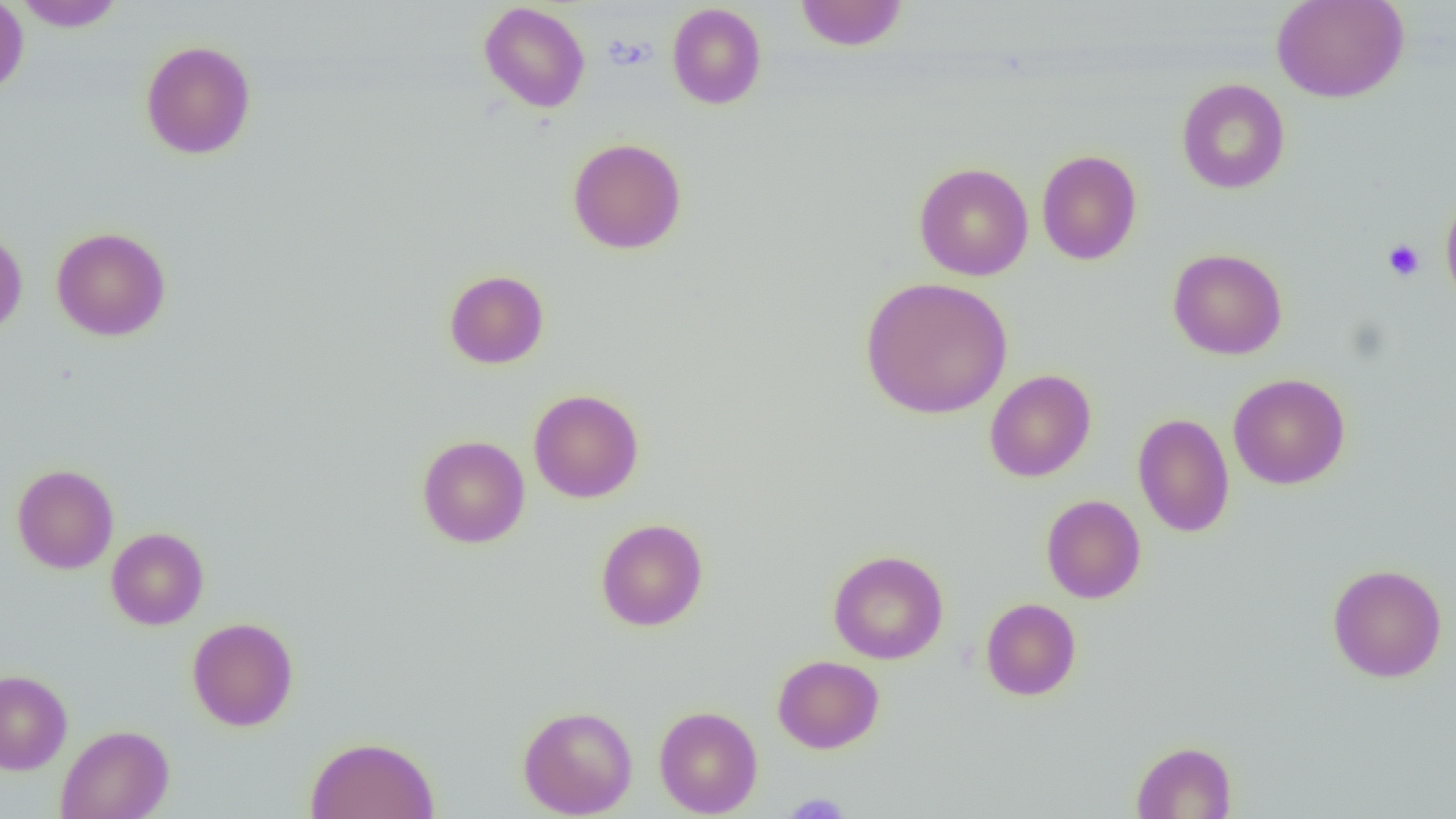
Summary:
  - Coordinate format: approximate bounding boxes as (x1,y1)-(x2,y2) corner pairs in pixels
  - Uninfected red blood cell locations: (0,0)-(29,96), (12,0)-(126,31), (795,0)-(907,51), (1271,0)-(1409,103), (479,2)-(590,112), (667,3)-(767,109), (140,40)-(256,159), (1176,78)-(1290,194), (568,137)-(687,254), (1036,150)-(1142,265), (914,162)-(1033,280), (1440,191)-(1456,312), (51,226)-(171,341), (0,229)-(27,337), (1168,248)-(1287,360), (444,270)-(548,369), (859,276)-(1013,420), (984,369)-(1096,482), (1228,373)-(1350,489), (528,389)-(644,503), (1133,413)-(1235,537), (417,435)-(530,548), (12,464)-(119,574), (1041,495)-(1146,603), (595,518)-(708,631), (106,527)-(209,630), (828,550)-(949,664), (1327,563)-(1447,683), (980,598)-(1082,701), (187,617)-(299,731), (772,655)-(884,754), (0,670)-(72,774), (518,704)-(638,818), (654,705)-(763,817), (56,724)-(174,819), (305,736)-(440,819), (1130,741)-(1237,818)
  - Platelet locations: (602,34)-(656,71), (1383,239)-(1425,281), (782,793)-(852,818)
  - Slide-level diagnosis: negative for blood parasites
  - Modality: light microscopy
  - Preparation: thin blood smear
  - Image size: 1456×819 pixels
  - Magnification: 1000x
  - Field of view: one of a larger specimen